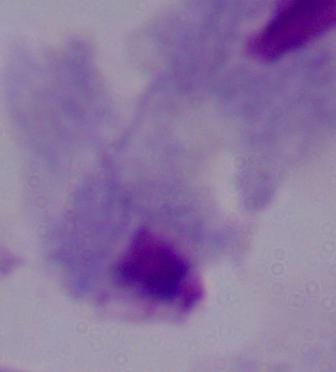

1000x magnification. Photomicrograph. A trichomonad is seen.